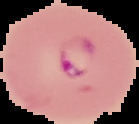
preparation = thin blood film
image size = 139×124 pixels
image type = segmented cell region with the area outside set to black
malaria status = parasitized